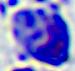

identification = leukocyte
magnification = 400x
modality = photomicrograph